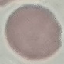

malaria status = uninfected
image type = automatically extracted cell patch, resized to 64 × 64 pixels
preparation = thin blood smear
stain = Giemsa
capture = smartphone through the microscope eyepiece